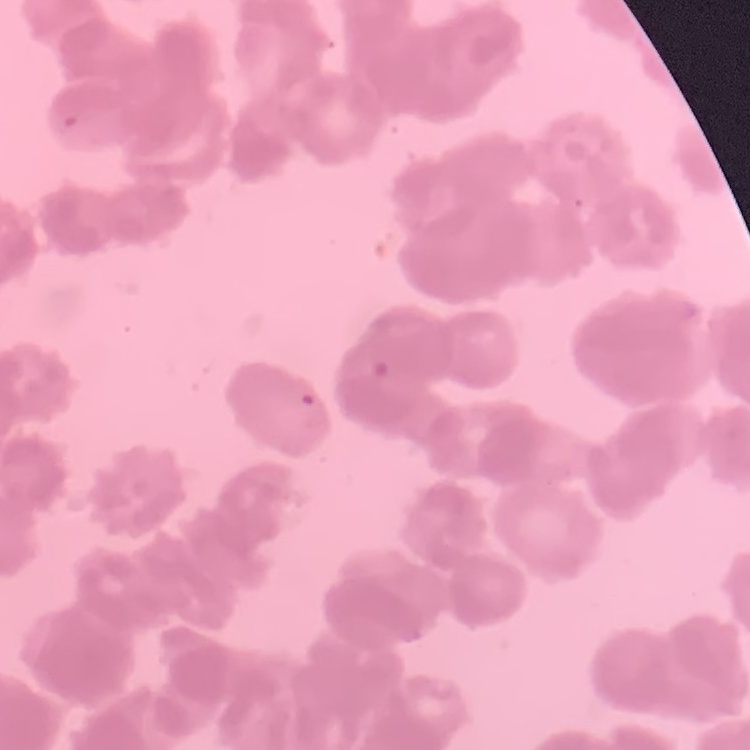

Summary:
  - Erythrocyte morphology: rouleaux formation
  - Preparation: thin peripheral smear
  - Stain: Field's or Giemsa
  - Image type: one tile cut from a larger photomicrograph